State the preparation type.
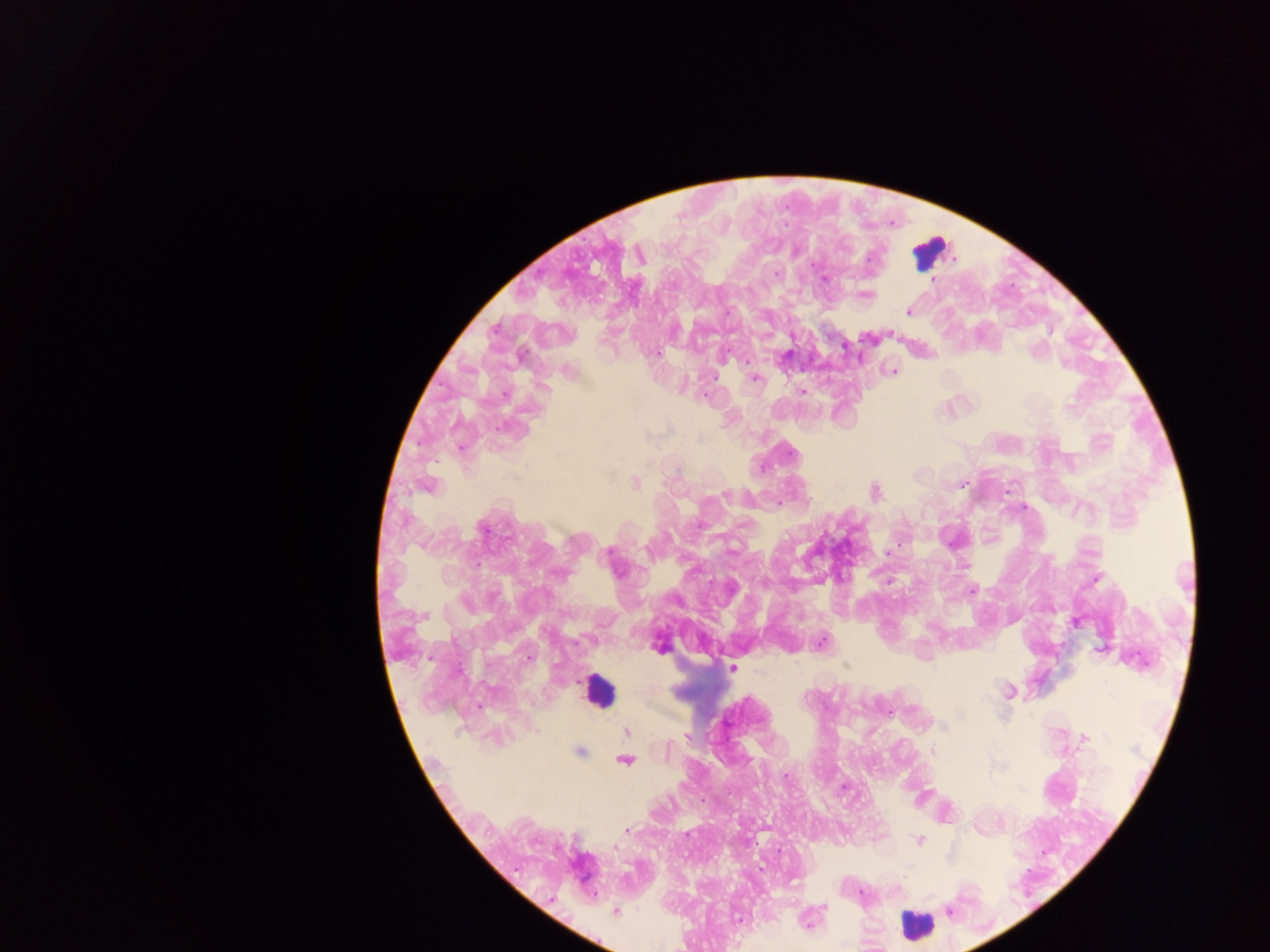
Thick blood smear.

Approximate centers as {x, y} in pixels.
Summary:
  - Leukocyte locations: {930, 252}, {598, 692}, {917, 926}
  - Malaria parasite locations: {869, 258}, {776, 273}, {825, 278}, {932, 280}, {867, 295}, {727, 312}, {908, 312}, {656, 353}, {748, 362}, {893, 371}, {754, 379}, {803, 391}, {504, 395}, {705, 396}, {1068, 407}, {461, 449}, {792, 452}, {635, 483}, {963, 484}, {427, 486}, {875, 492}, {725, 495}, {483, 529}, {901, 543}, {609, 553}, {888, 553}, {967, 566}, {1096, 580}, {972, 591}, {1076, 622}, {822, 642}, {659, 647}, {429, 658}, {528, 658}, {846, 666}, {732, 668}, {1009, 692}, {479, 706}, {944, 726}, {536, 730}, {627, 732}, {687, 737}, {1084, 739}, {580, 751}, {934, 752}, {625, 761}, {786, 776}, {627, 830}, {920, 841}, {615, 847}, {862, 893}, {823, 907}, {950, 911}, {616, 912}, {740, 920}, {808, 923}
  - Field of view: single
  - Image size: 1270×952 pixels
  - Capture: mobile-phone photograph through a microscope
  - Country: Ghana